Report the malaria status.
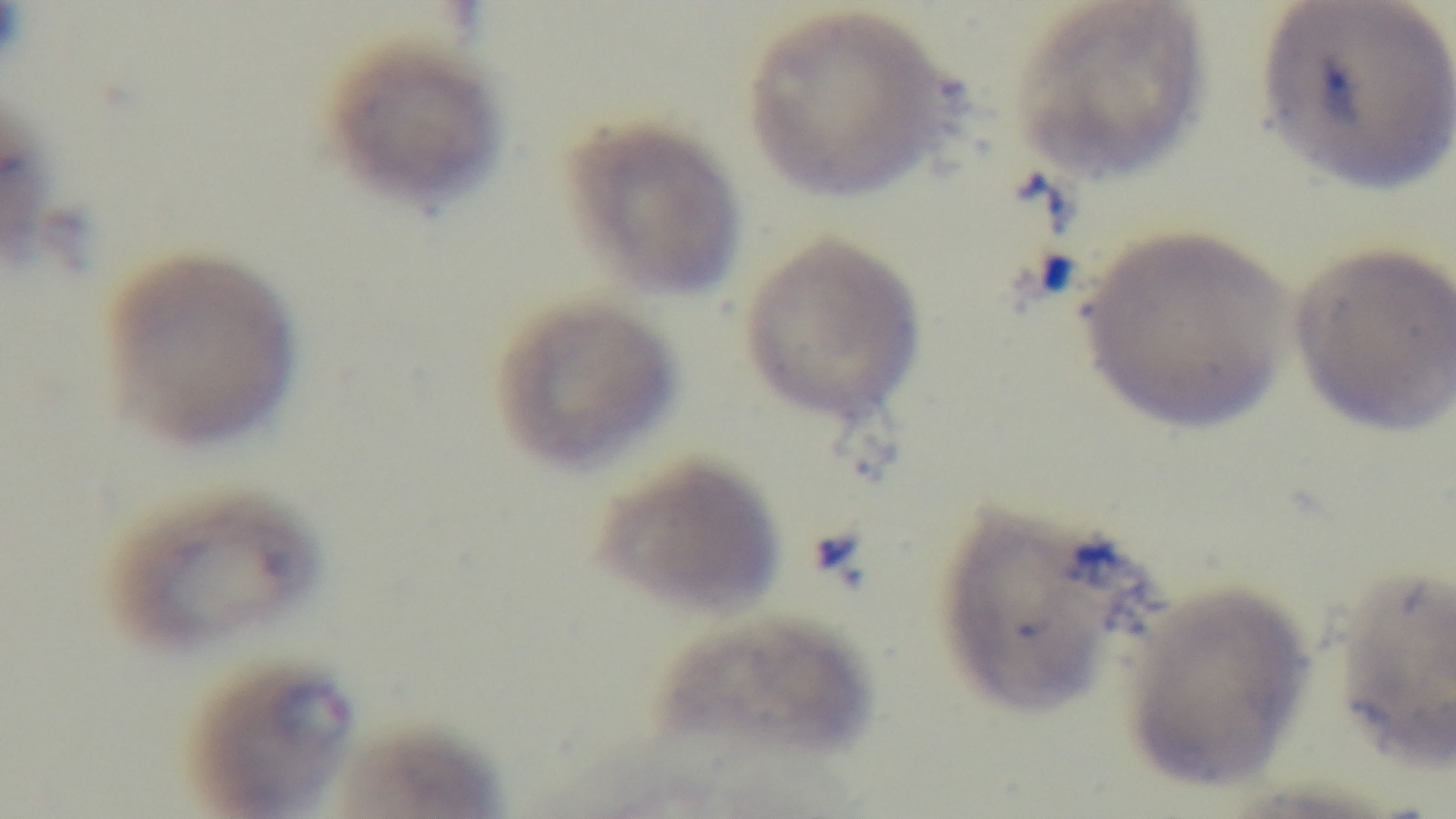

Infected.

{
  "objective": "100x oil immersion",
  "field_of_view": "single",
  "capture": "mounted 4K digital camera",
  "modality": "light microscopy",
  "stain": "Giemsa",
  "preparation": "thin smear"
}